Outline each blood parasite and name the species.
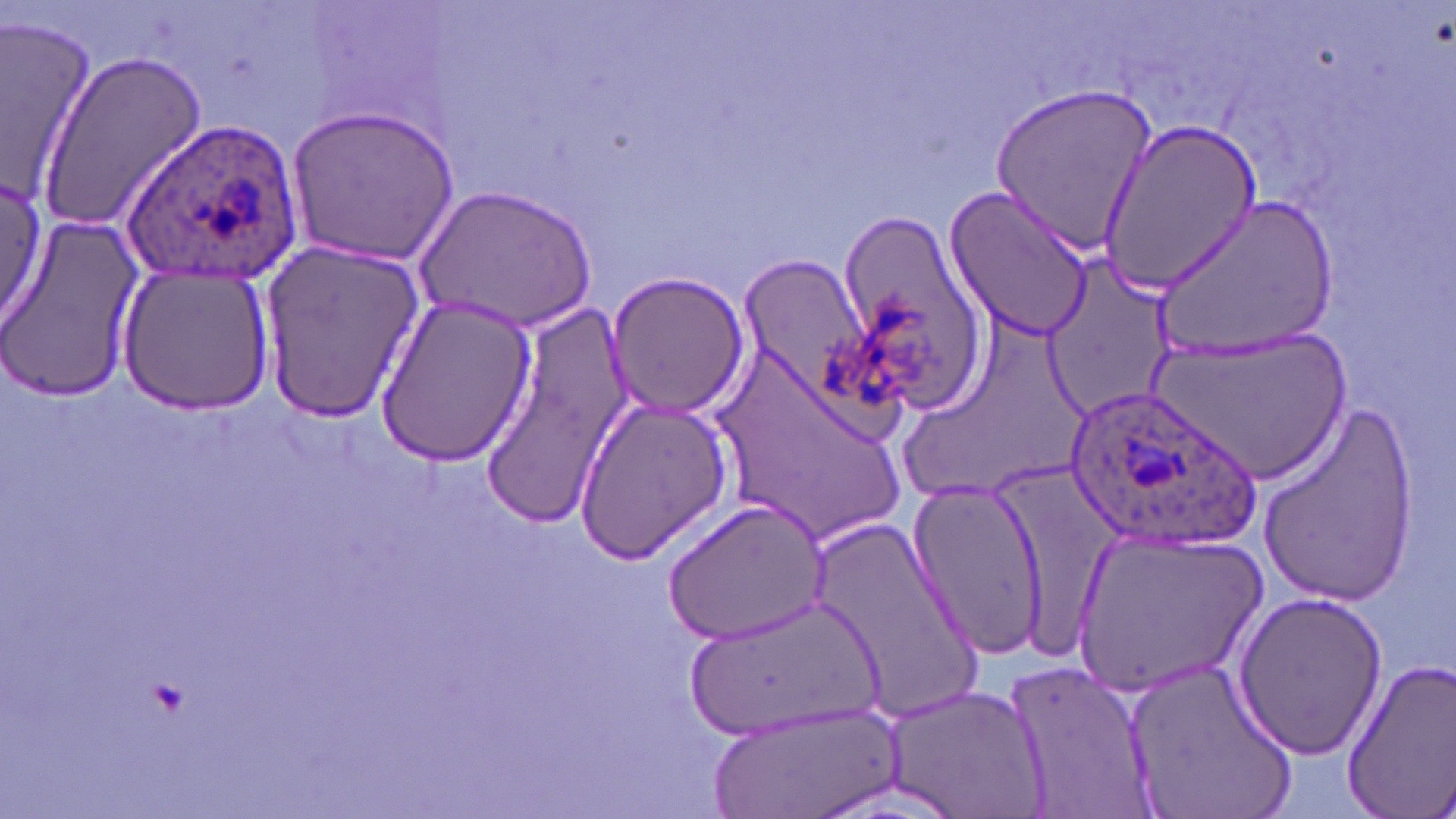
Approximate bounding boxes as (x1, y1, x2, y2) in pixels.
Plasmodium ovale-infected red blood cells: (122, 115, 304, 285), (1062, 386, 1257, 552).
No Plasmodium falciparum, Plasmodium malariae, Plasmodium vivax, Babesia divergens, or Trypanosoma brucei observed.

Uninfected red blood cell locations: (0, 16, 104, 209), (36, 52, 208, 232), (990, 84, 1156, 255), (287, 102, 462, 267), (1098, 121, 1260, 292), (0, 172, 47, 332), (944, 180, 1098, 343), (419, 184, 598, 333), (1153, 194, 1343, 358), (833, 210, 994, 417), (3, 215, 149, 408), (259, 241, 422, 422), (735, 254, 873, 401), (1046, 254, 1174, 413), (116, 260, 274, 415), (605, 271, 752, 421), (372, 291, 539, 466), (477, 301, 633, 521), (702, 329, 917, 551), (1150, 332, 1355, 487), (572, 395, 735, 563), (1256, 398, 1421, 603), (907, 477, 1049, 655), (663, 498, 826, 646), (808, 507, 985, 726), (1068, 528, 1269, 696), (1231, 588, 1389, 761), (680, 591, 888, 742), (1123, 650, 1299, 819), (1003, 654, 1154, 819), (1344, 657, 1456, 810), (880, 686, 1047, 815), (705, 701, 906, 819). Slide-level diagnosis: Plasmodium ovale. Image is 1456×819 pixels. 1000x magnification. One field of a larger specimen. May-Grünwald-Giemsa-stained preparation. Light microscopy. Thin blood smear.